Report the malaria status of this cell.
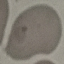

Uninfected.

Giemsa-stained preparation. Cell patch, automatically extracted from a larger field of view and resized to 64 × 64 pixels. Thin blood smear. Photographed with a smartphone camera at the microscope eyepiece.